Report the malaria status of this cell.
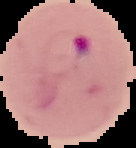
It is parasitized.

Summary:
  - Preparation: thin blood smear
  - Image type: cell region segmented out of the field of view; surrounding area masked to black
  - Image size: 136×148 pixels